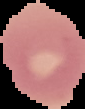
Summary:
  - Preparation: thin blood film
  - Image size: 85×109 pixels
  - Image type: segmented cell region on a black background
  - Result: no malaria parasites seen